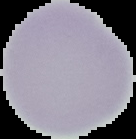
Summary:
  - Preparation: thin blood smear
  - Malaria status: uninfected
  - Image type: segmented cell region on a black background
  - Image size: 136×139 pixels